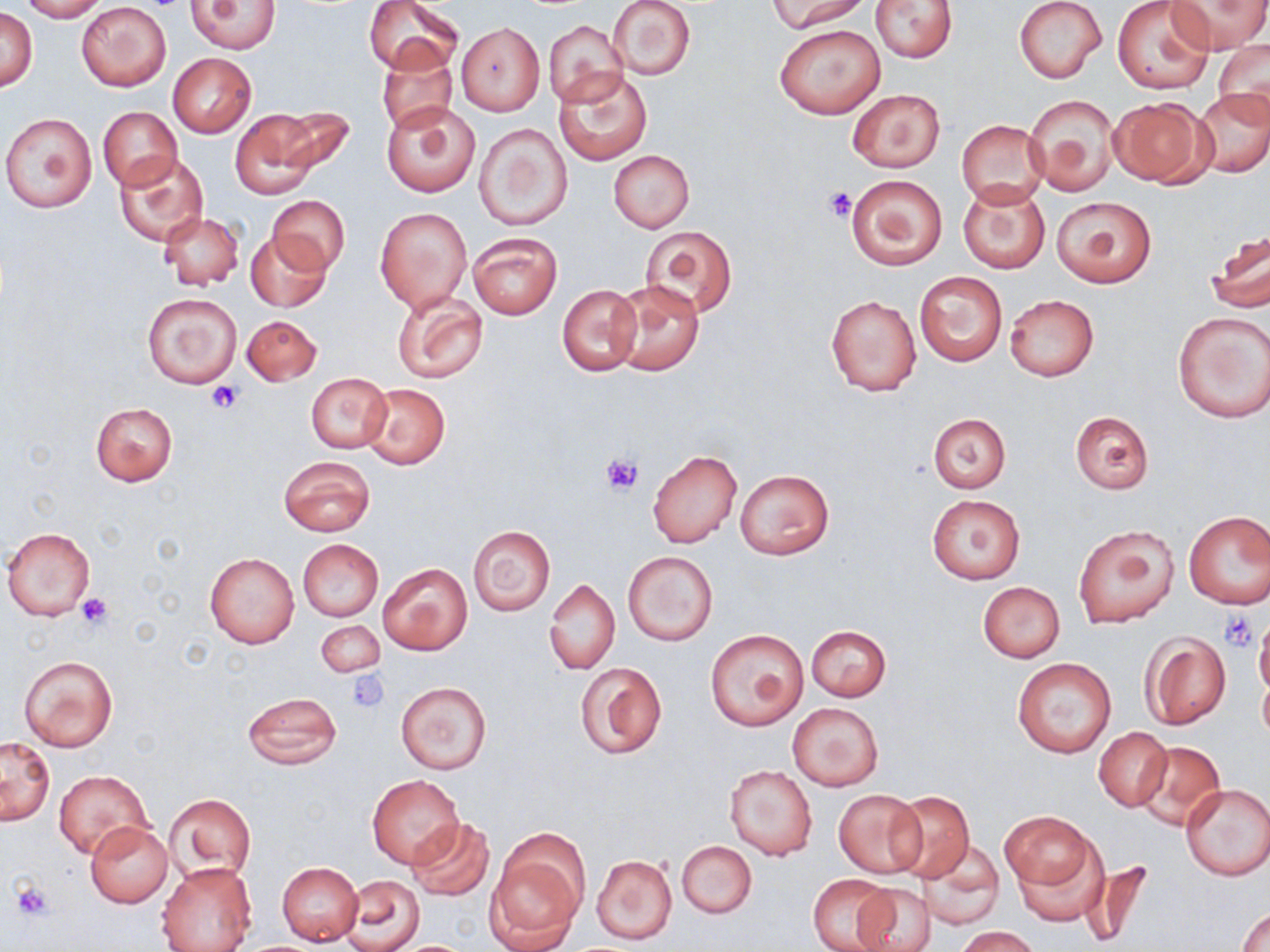
Approximate bounding boxes as (x1,y1)-(x2,y2) corner pairs in pixels. Platelet locations: (823,185)-(856,223), (207,381)-(242,414), (602,452)-(645,497), (75,593)-(115,632), (1220,611)-(1259,651), (348,671)-(389,715), (9,878)-(55,922). Uninfected red blood cell locations: (18,0)-(109,21), (607,0)-(696,81), (767,0)-(870,33), (1014,0)-(1107,84), (1169,0)-(1268,54), (188,1)-(281,53), (364,1)-(461,73), (871,1)-(957,63), (1112,1)-(1215,94), (77,2)-(170,91), (1,8)-(37,92), (544,20)-(626,108), (775,22)-(886,120), (456,23)-(544,115), (1213,41)-(1270,125), (377,47)-(457,136), (168,53)-(256,137), (552,68)-(651,166), (1193,88)-(1270,176), (847,89)-(945,172), (1025,94)-(1119,196), (1109,96)-(1213,187), (382,102)-(480,197), (98,106)-(181,190), (272,107)-(355,178), (231,109)-(321,200), (2,112)-(97,212), (956,119)-(1048,208), (475,123)-(572,231), (608,150)-(694,231), (113,151)-(210,247), (846,174)-(947,270), (957,180)-(1050,275), (267,195)-(349,275), (1050,196)-(1156,288), (375,208)-(470,311), (157,211)-(244,290), (640,225)-(737,318), (1207,229)-(1269,316), (246,232)-(331,312), (467,232)-(562,320), (913,271)-(1008,367), (609,279)-(704,376), (558,284)-(642,376), (390,287)-(488,386), (142,292)-(242,389), (826,295)-(921,396), (1005,295)-(1098,381), (1173,312)-(1270,423), (243,313)-(322,387), (305,373)-(393,454), (362,383)-(450,469), (90,403)-(177,486), (1069,410)-(1153,494), (926,413)-(1011,492), (647,448)-(742,549), (279,455)-(377,536), (734,468)-(834,559), (926,494)-(1026,584), (1183,511)-(1269,608), (1073,524)-(1178,627), (3,526)-(96,620), (469,526)-(555,615), (296,538)-(383,622), (624,550)-(717,645), (203,553)-(299,648), (378,562)-(472,656), (545,578)-(619,675), (978,581)-(1064,663), (1253,615)-(1270,699), (317,620)-(384,678), (805,625)-(891,701), (705,629)-(808,731), (1141,632)-(1232,730), (19,654)-(118,752), (1012,657)-(1117,758), (573,660)-(666,761), (396,682)-(491,774), (241,691)-(343,770), (787,702)-(884,791), (1092,726)-(1172,811), (1,737)-(55,825), (1133,740)-(1225,831), (724,765)-(817,860), (54,770)-(151,860), (367,775)-(464,869), (1179,781)-(1270,880), (832,788)-(925,877), (887,791)-(974,883), (165,793)-(256,882), (1002,811)-(1101,918), (407,817)-(495,901), (84,820)-(173,908), (677,841)-(757,918), (919,841)-(1004,930), (485,842)-(585,952), (592,855)-(677,944), (157,861)-(256,952), (277,862)-(363,944), (808,874)-(899,952), (343,875)-(424,951), (851,882)-(934,952), (1237,905)-(1270,951), (955,927)-(1040,952). Slide-level diagnosis: negative for blood parasites. Single field of view. Image is 1270×952 pixels. Thin blood smear. 1000x magnification. May-Grünwald-Giemsa-stained preparation. Optical microscopy.